Report the malaria status of this cell.
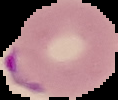

It is parasitized.

image size = 118×100 pixels
image type = segmented cell region with the area outside set to black
preparation = thin blood film